Comment on the morphology of the red blood cells.
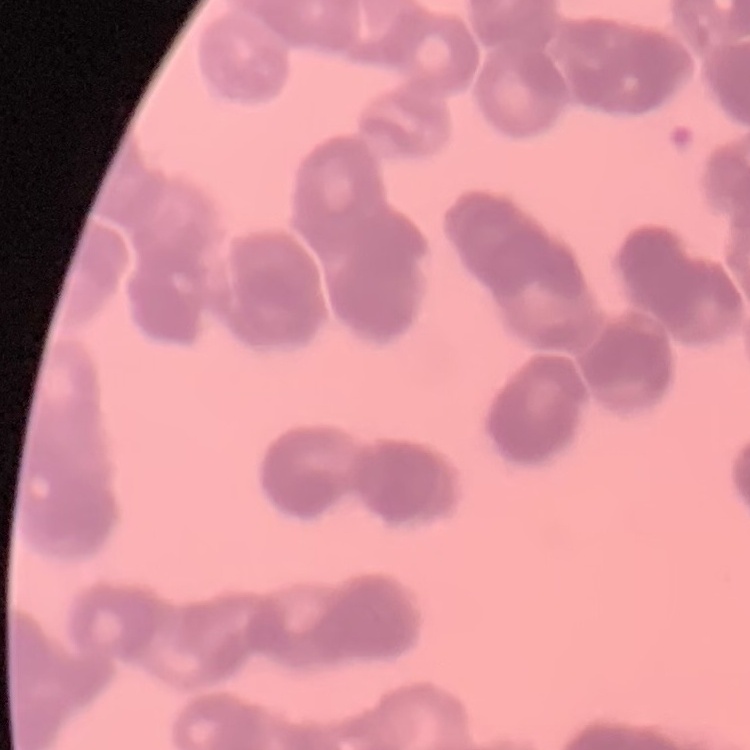

They show rouleaux formation.

Square crop of a larger photomicrograph. Thin blood smear. Stained with either Field's or Giemsa.